Assess the morphology of the erythrocytes.
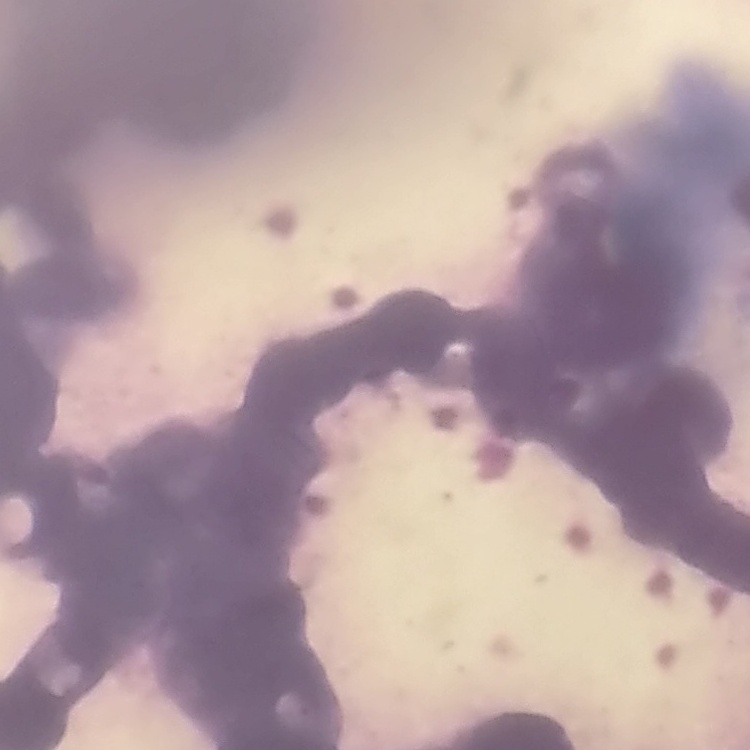

They show rouleaux formation.

Field's or Giemsa stain. Square crop of a larger photomicrograph. Thin peripheral smear.